Identify the cell.
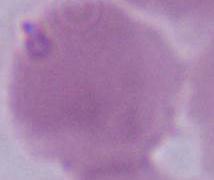

An erythrocyte.

modality: photomicrograph
magnification: 1000x